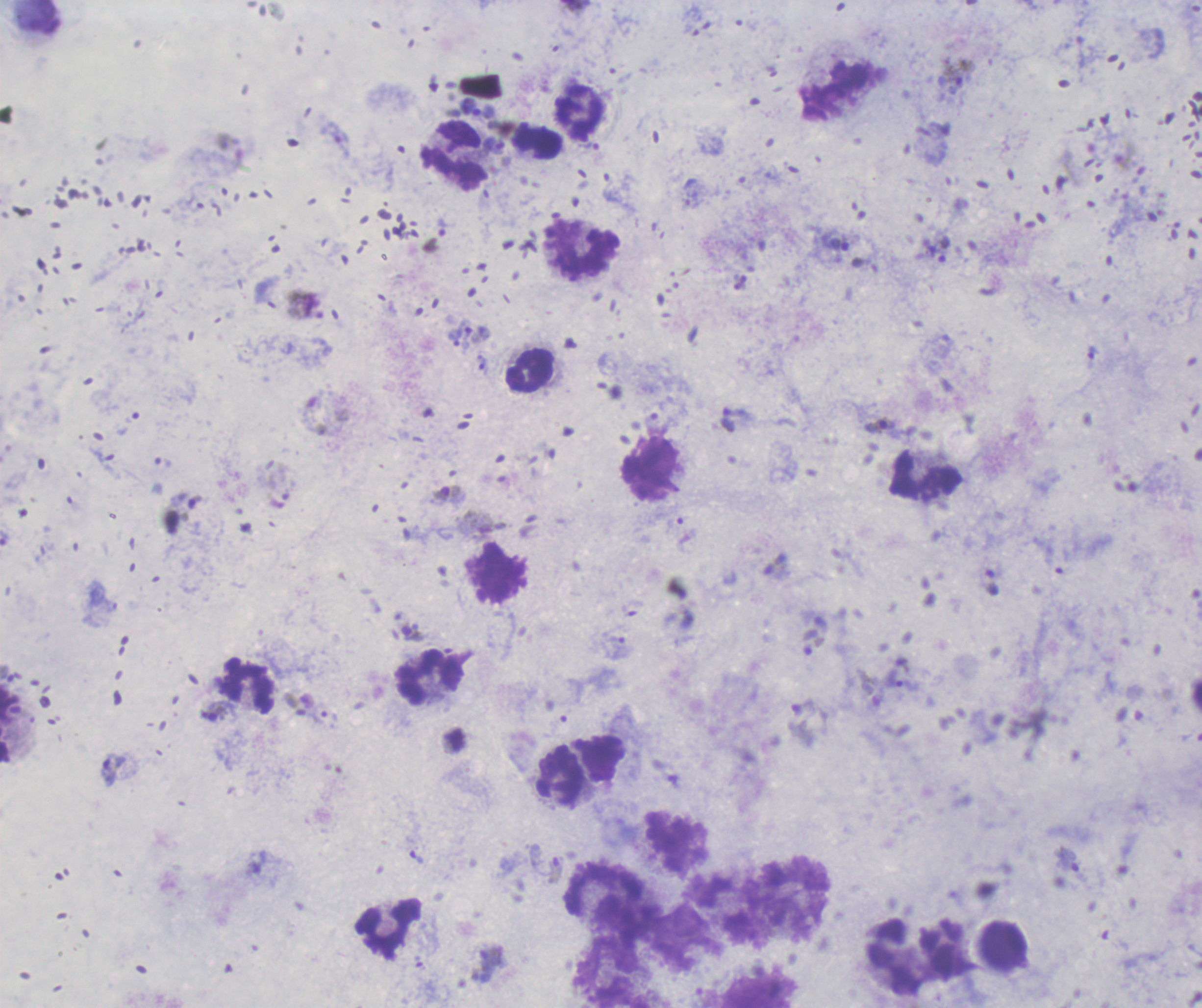
Approximate centers as (x, y) in pixels. Trophozoite locations: (959, 74), (479, 109), (495, 145), (456, 337), (621, 648), (903, 681), (113, 771). Leukocyte locations: (836, 90), (579, 112), (538, 142), (454, 167), (583, 249), (528, 370), (650, 468), (925, 478), (431, 678), (249, 689), (561, 774), (390, 927), (1003, 946), (895, 956), (609, 972). Gametocyte locations: (880, 425), (450, 494), (412, 633), (214, 713), (556, 870), (490, 964). Life-cycle stages observed: trophozoite, gametocyte. Romanowsky-stained preparation. Captured at 100x magnification. Previously used in an actual diagnosis. One field from this slide. Image is 1202×1008 pixels. Background quality: good. Thick blood film. Result: positive for Plasmodium parasites.